Outline each Plasmodium malariae-infected red blood cell.
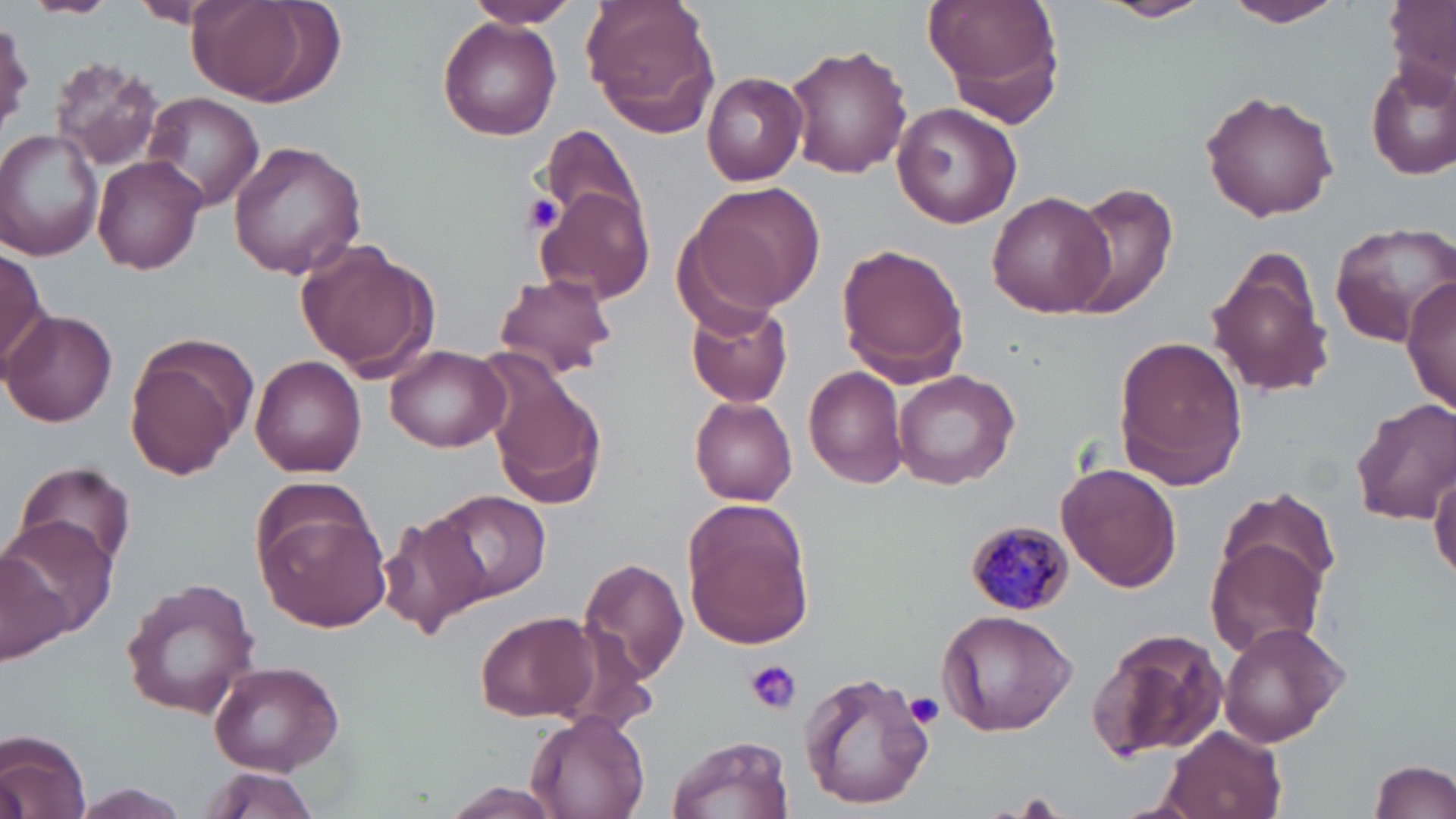
Approximate bounding boxes as (x1, y1, x2, y2) in pixels.
Plasmodium malariae-infected red blood cells: (965, 523, 1073, 613).

slide-level diagnosis = Plasmodium malariae
magnification = 1000x
uninfected red blood cell locations = approximate bounding boxes as (x1, y1, x2, y2) in pixels: (20, 0, 116, 18), (129, 0, 226, 30), (183, 0, 343, 110), (465, 0, 580, 29), (581, 0, 721, 135), (920, 0, 1064, 109), (1096, 0, 1213, 23), (1224, 0, 1349, 29), (1383, 0, 1456, 91), (438, 15, 563, 140), (0, 16, 33, 133), (783, 42, 912, 179), (47, 56, 164, 174), (1366, 58, 1456, 182), (702, 72, 809, 185), (1201, 90, 1340, 221), (142, 93, 265, 210), (891, 102, 1022, 229), (544, 125, 643, 230), (0, 129, 105, 260), (227, 139, 367, 279), (92, 155, 209, 275), (687, 183, 825, 316), (1062, 184, 1179, 315), (533, 185, 656, 306), (986, 192, 1114, 318), (1330, 220, 1456, 347), (295, 241, 437, 380), (837, 243, 969, 383), (1206, 245, 1335, 399), (0, 246, 53, 369), (491, 272, 618, 380), (1403, 277, 1454, 419), (686, 303, 794, 407), (3, 310, 116, 426), (122, 333, 257, 478), (1113, 335, 1247, 489), (386, 344, 511, 452), (249, 355, 367, 476), (485, 363, 608, 514), (804, 366, 909, 489), (892, 369, 1020, 492), (688, 396, 799, 505), (1350, 398, 1456, 527), (12, 460, 138, 573), (1059, 463, 1182, 592), (1430, 468, 1456, 583), (1213, 486, 1341, 607), (433, 490, 548, 603), (684, 501, 814, 650), (252, 502, 392, 631), (379, 512, 489, 639), (3, 515, 119, 642), (1204, 535, 1331, 661), (0, 546, 72, 665), (578, 556, 691, 684), (119, 576, 262, 719), (937, 609, 1077, 738), (472, 610, 602, 724), (1217, 622, 1348, 749), (1090, 627, 1231, 761), (209, 659, 345, 773), (799, 669, 935, 810), (526, 709, 651, 819), (1160, 723, 1287, 819), (1, 730, 92, 818), (668, 735, 794, 819), (1368, 759, 1456, 819), (197, 766, 322, 818), (1, 767, 31, 819), (69, 782, 194, 816), (443, 784, 559, 819)
preparation = thin blood film
field of view = single
platelet locations = approximate bounding boxes as (x1, y1, x2, y2) in pixels: (521, 192, 565, 234), (746, 661, 800, 714), (906, 693, 942, 727)
image size = 1456×819 pixels
stain = May-Grünwald-Giemsa
modality = optical microscopy